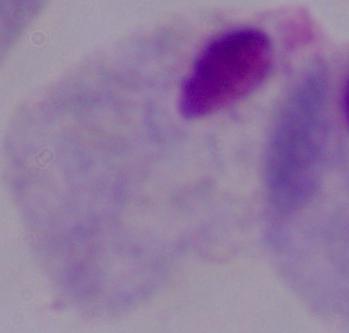

Summary:
  - Magnification: 1000x
  - Identification: trichomonad
  - Modality: micrograph